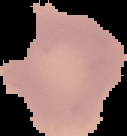
Summary:
  - Malaria status: uninfected
  - Image type: segmented cell region on a black background
  - Preparation: thin blood smear
  - Image size: 127×136 pixels